Classify this cell by malaria status.
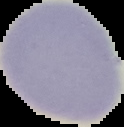

Uninfected.

From a thin blood smear. Image is 124×127 pixels. The area outside the segmented cell region is set to black.